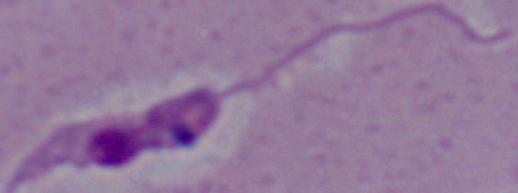
identification = Leishmania
magnification = 1000x
modality = micrograph